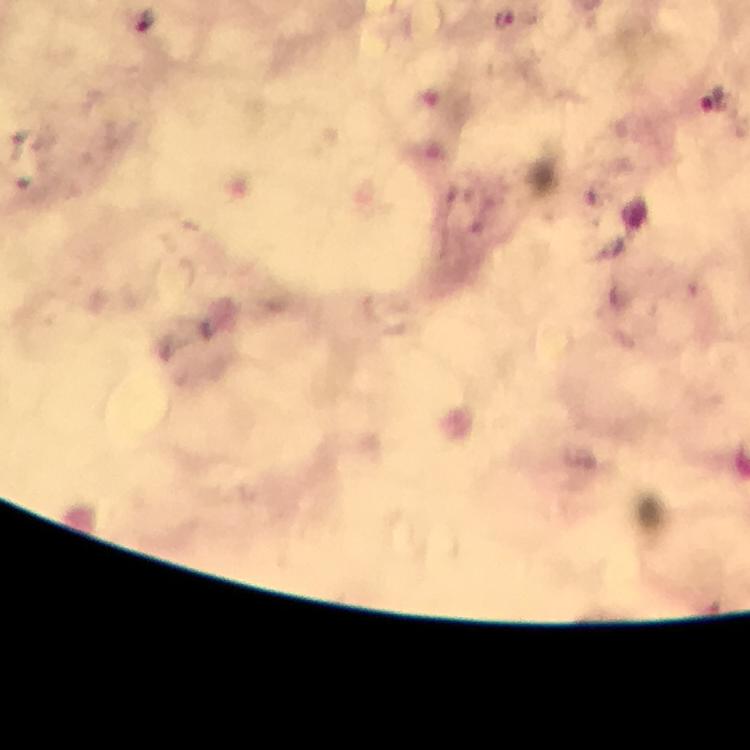 Approximate centers as {x, y} in pixels. Plasmodium parasite locations: {504, 16}, {146, 20}, {714, 101}. 100x magnification. Thick smear. Image is 750×750 pixels. Immersion oil was used. From a malaria diagnostic workup. Photographed through the microscope with a smartphone camera. A crop from one field of view. Giemsa stain.